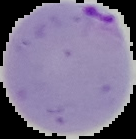
preparation: thin blood film
image_type: segmented cell region with the area outside set to black
image_size: 136×139 pixels
result: malaria parasites identified